Identify the parasite.
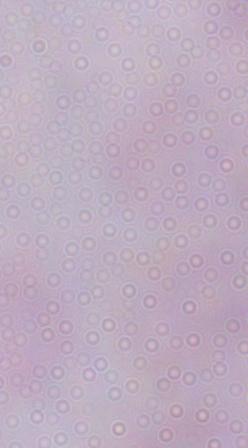

This is a trypanosome.

{
  "magnification": "1000x",
  "modality": "photomicrograph"
}